Identify the preparation type.
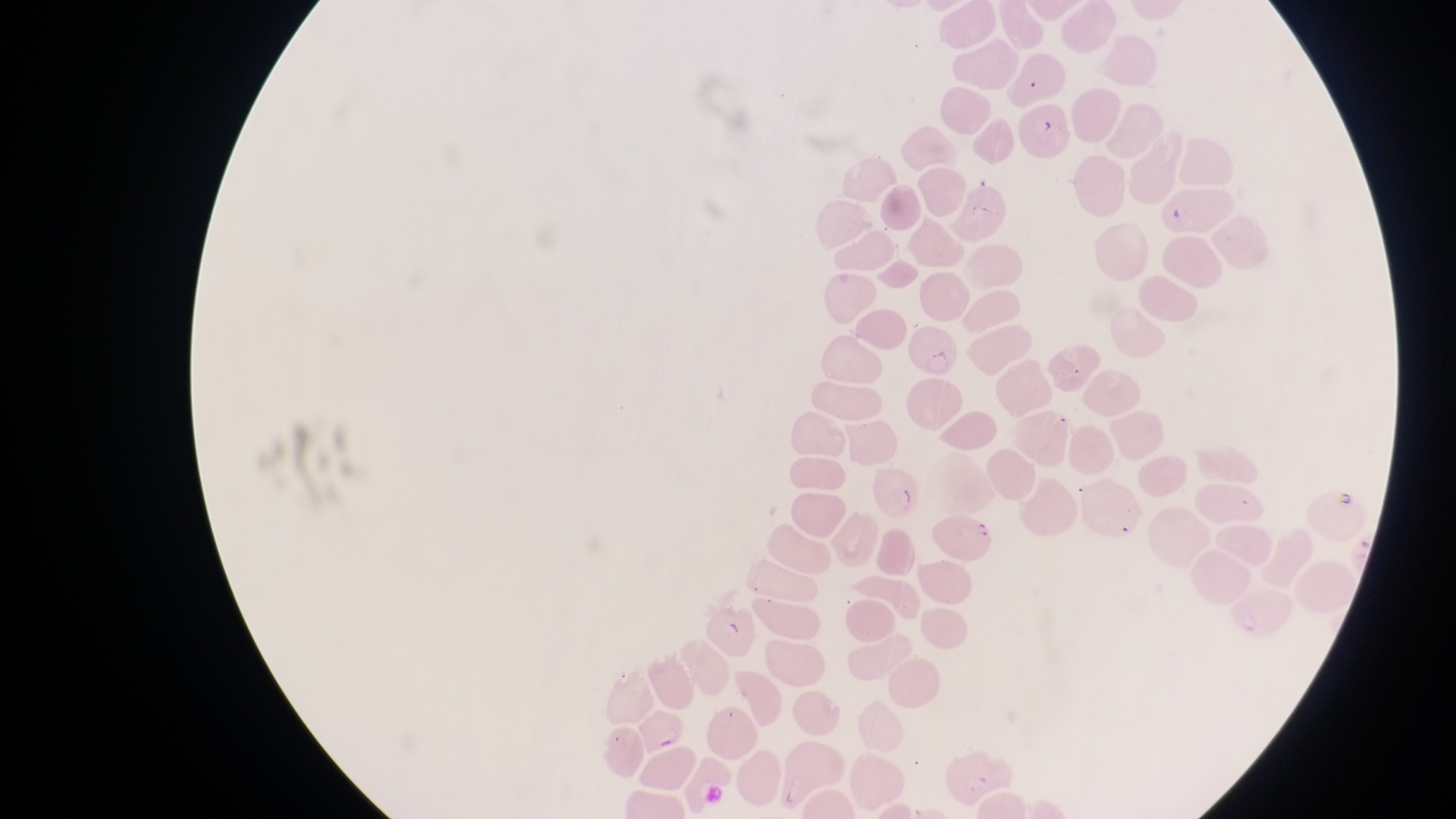

Thin blood smear.

Approximate bounding boxes as [left, top, right, bottom] in pixels. Parasitised red blood cell locations: [1020, 98, 1076, 162], [909, 325, 961, 381], [868, 459, 923, 522], [938, 510, 997, 560], [642, 708, 692, 754]. Single field of view. Magnification of 1000x. Sample from Uganda. Photographed through the eyepiece of an Olympus CX-23 microscope with a smartphone camera. Image is 1456×819 pixels.